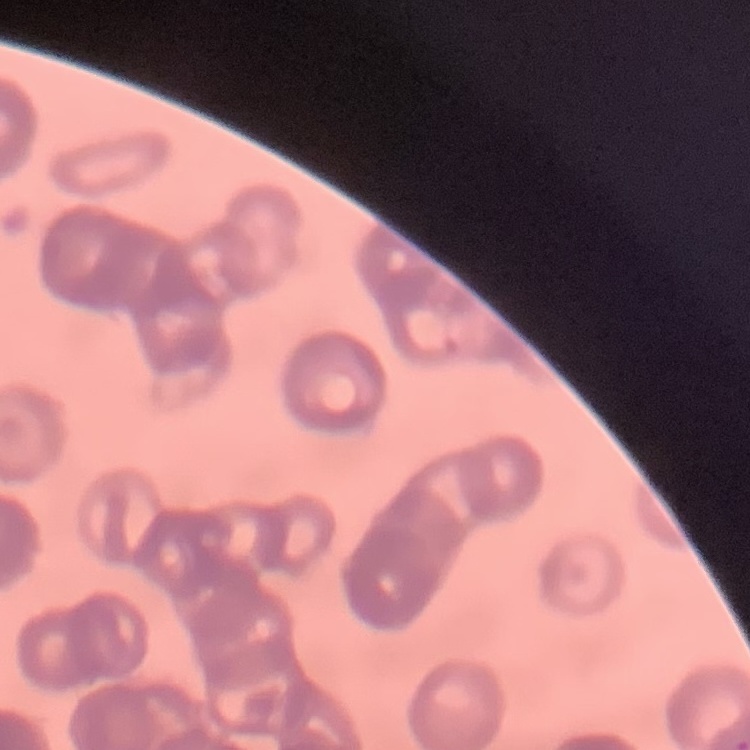

erythrocyte morphology = rouleaux formation
stain = Field's or Giemsa
preparation = thin peripheral smear
image type = one tile cut from a larger photomicrograph